Assess this cell for malaria.
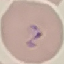
It is parasitized.

preparation = thin blood smear
stain = Giemsa
image type = automatically extracted cell patch, resized to 64 × 64 pixels
capture = smartphone through the microscope eyepiece